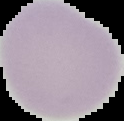
Summary:
  - Preparation: thin blood smear
  - Malaria status: uninfected
  - Image type: segmented cell region with the area outside set to black
  - Image size: 124×121 pixels